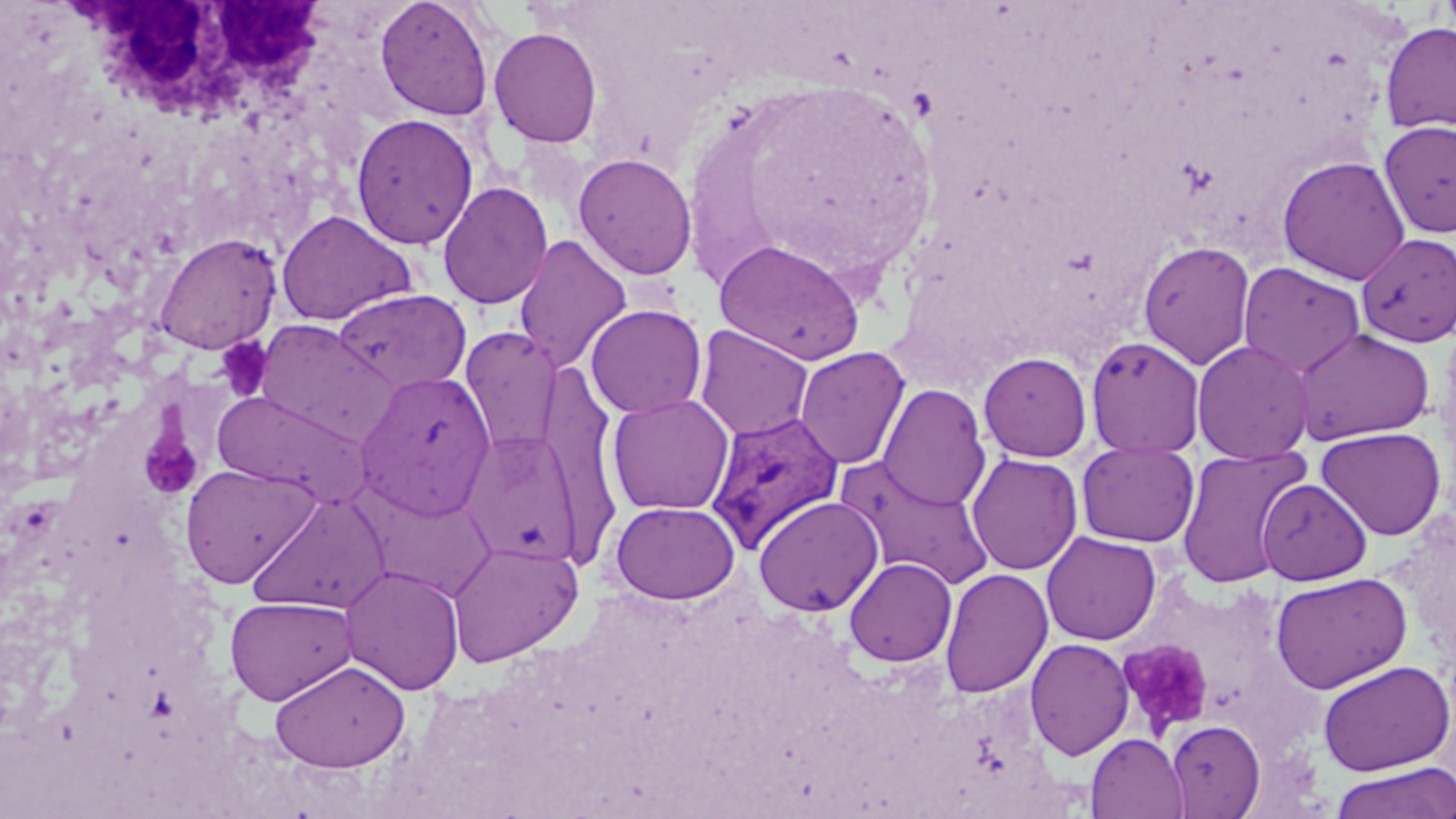

slide-level diagnosis = Plasmodium vivax
uninfected red blood cell locations = approximate bounding boxes as (x1, y1, x2, y2) in pixels: (375, 0, 494, 121), (1379, 22, 1456, 134), (488, 26, 602, 148), (350, 112, 479, 250), (1378, 119, 1456, 238), (573, 152, 698, 281), (1277, 155, 1411, 285), (437, 181, 553, 310), (276, 210, 417, 325), (152, 232, 282, 354), (1356, 232, 1456, 348), (513, 233, 632, 373), (714, 239, 866, 365), (1137, 240, 1256, 371), (1238, 261, 1366, 379), (331, 288, 472, 395), (585, 303, 707, 418), (253, 320, 399, 448), (693, 324, 814, 441), (460, 326, 563, 458), (1293, 327, 1435, 445), (1086, 335, 1205, 458), (1191, 339, 1315, 464), (793, 346, 912, 470), (978, 351, 1093, 462), (355, 371, 496, 520), (877, 384, 991, 512), (213, 390, 371, 508), (607, 394, 735, 515), (1315, 426, 1446, 540), (460, 429, 583, 565), (1075, 440, 1199, 548), (1175, 445, 1312, 588), (966, 452, 1083, 576), (835, 456, 995, 589), (179, 462, 319, 588), (1256, 478, 1372, 585), (247, 491, 392, 615), (754, 496, 884, 617), (610, 501, 740, 604), (1041, 531, 1161, 646), (446, 539, 583, 667), (844, 557, 957, 667), (340, 565, 465, 695), (940, 567, 1053, 698), (1271, 572, 1413, 693), (225, 595, 357, 706), (1024, 637, 1135, 760), (270, 659, 410, 772), (1317, 660, 1455, 776), (1165, 719, 1265, 818), (1086, 733, 1188, 819), (1329, 762, 1456, 819)
white blood cell locations = approximate bounding boxes as (x1, y1, x2, y2) in pixels: (67, 0, 328, 112)
modality = light microscopy
field of view = one of a larger specimen
magnification = 1000x
image size = 1456×819 pixels
Plasmodium vivax-infected red blood cell locations = approximate bounding boxes as (x1, y1, x2, y2) in pixels: (705, 410, 845, 554)
stain = May-Grünwald-Giemsa
platelet locations = approximate bounding boxes as (x1, y1, x2, y2) in pixels: (215, 336, 273, 401), (134, 419, 198, 499), (1119, 640, 1213, 736)
preparation = thin blood film